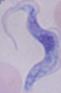

modality: photomicrograph
magnification: 1000x
identification: trypanosome